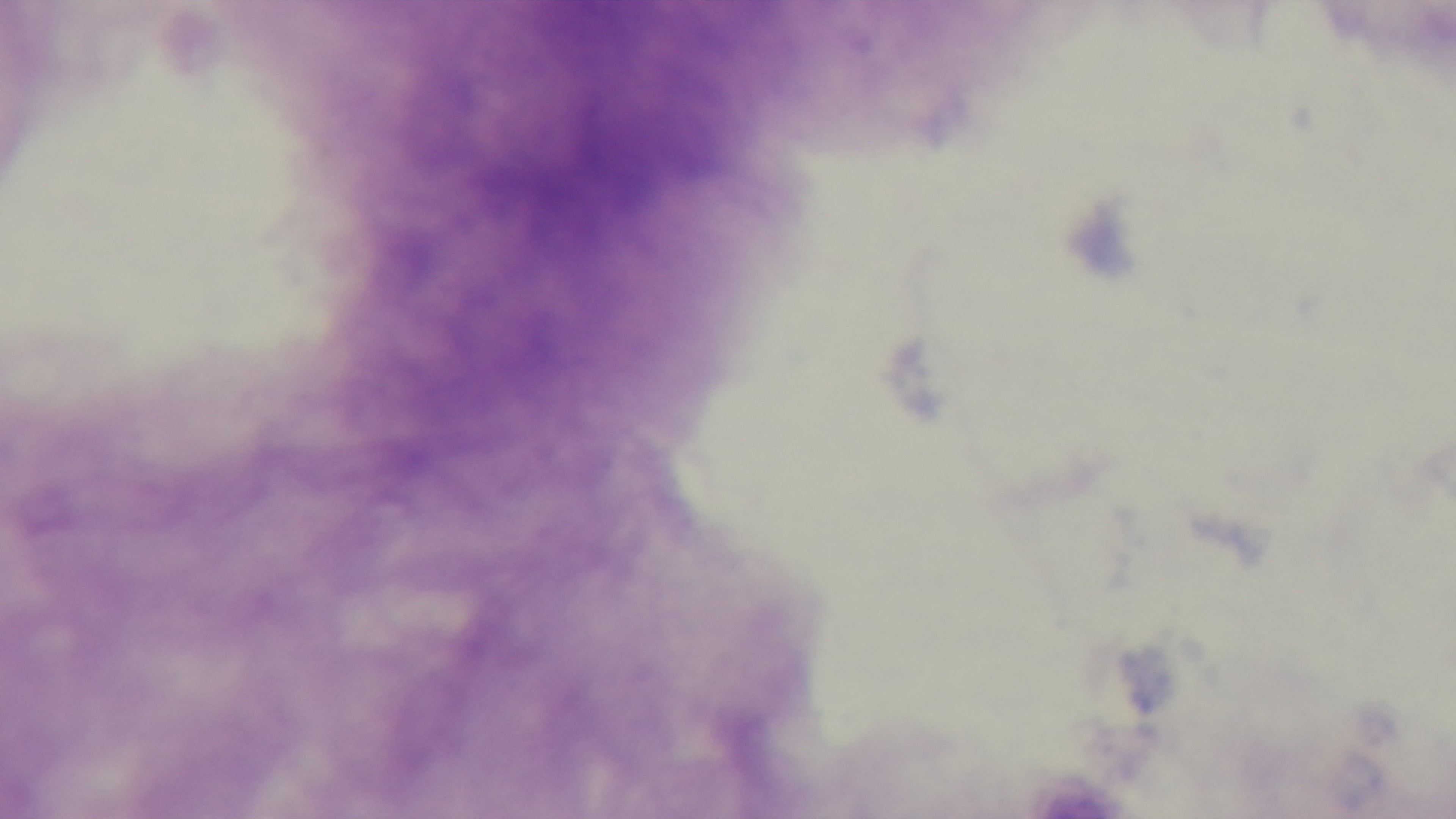
{
  "field_of_view": "single",
  "modality": "light microscopy",
  "objective": "100x oil immersion",
  "malaria_status": "negative",
  "preparation": "thick smear",
  "stain": "Giemsa",
  "capture": "mounted 4K digital camera"
}